Classify this cell by malaria status.
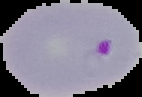

It is parasitized.

Image is 142×97 pixels. From a thin blood film. The area outside the segmented cell region is set to black.